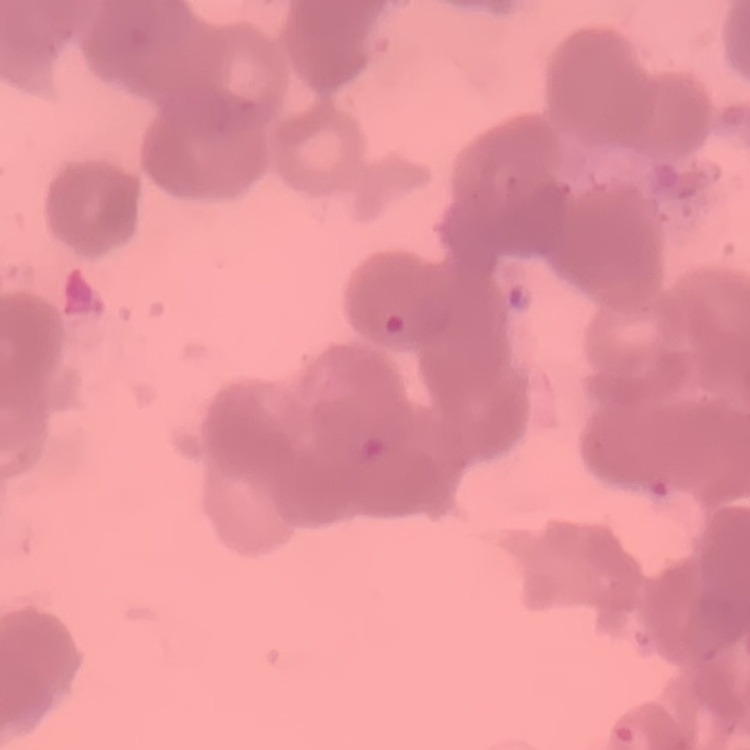

Summary:
  - Erythrocyte morphology: rouleaux formation
  - Preparation: thin blood film
  - Image type: square crop of a larger photomicrograph
  - Stain: Field's or Giemsa